Point out every malaria parasite and every leukocyte.
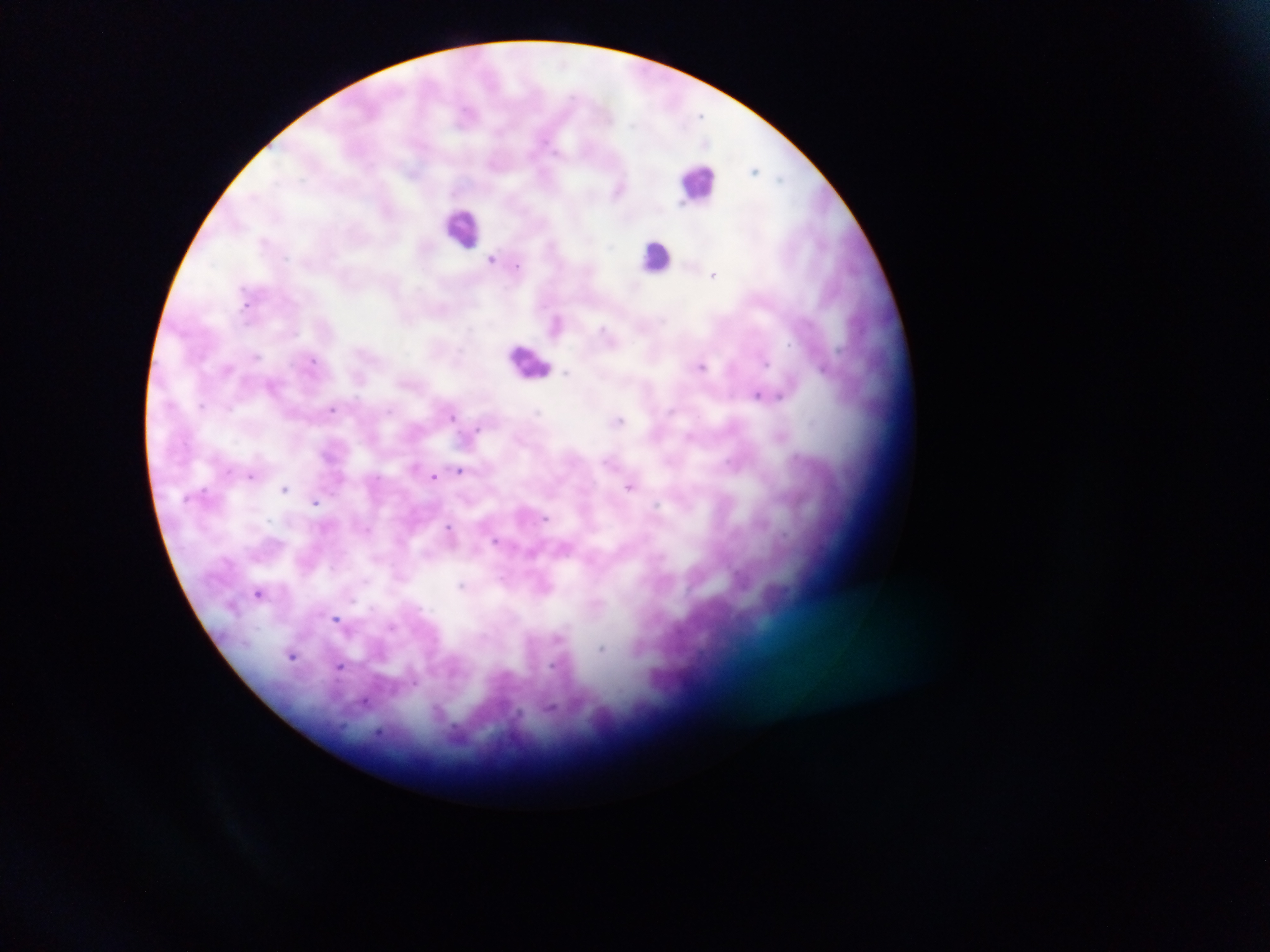
Approximate centers as x y in pixels.
Malaria parasites: 756 169; 620 189; 492 259; 714 274; 558 324; 703 366; 759 394; 332 409; 452 415; 619 420; 460 471; 251 476; 435 476; 631 487; 285 488; 315 501; 451 531; 497 541; 465 585; 259 592; 336 619; 292 655; 340 666; 365 702.
Leukocytes: 699 181; 464 228; 657 257; 530 361.

Collected in Ghana. Thick blood film. Mobile-phone photograph taken through the microscope. Image is 1270×952 pixels. One field of view.